Assess the morphology of the erythrocytes.
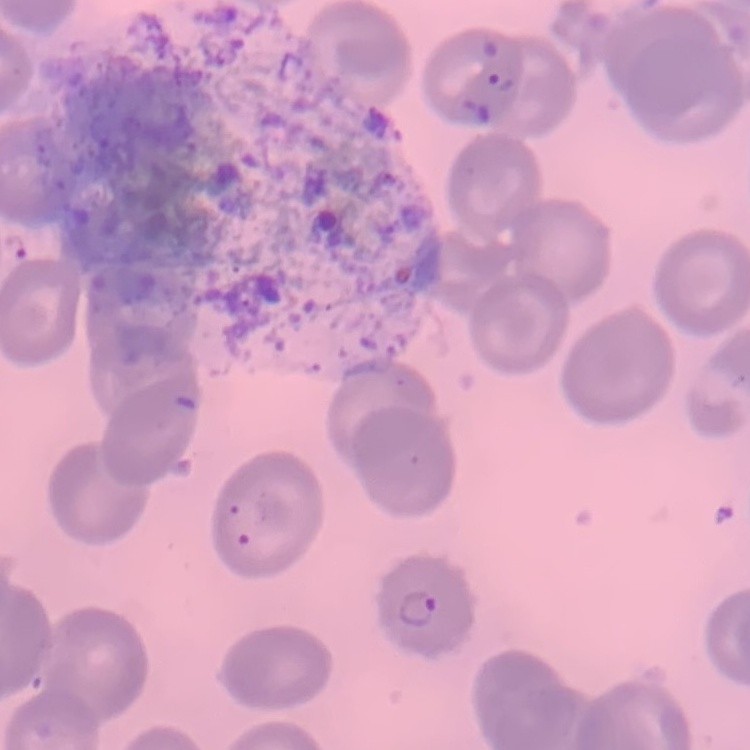
They show no rouleaux formation.

{
  "preparation": "thin blood smear",
  "stain": "Field's or Giemsa",
  "image_type": "square crop of a larger photomicrograph"
}